Classify this cell by malaria status.
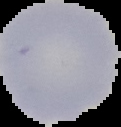

It is uninfected.

{
  "image_size": "121×127 pixels",
  "preparation": "thin blood smear",
  "image_type": "cell region segmented out of the field of view; surrounding area masked to black"
}